Locate and identify every blood parasite.
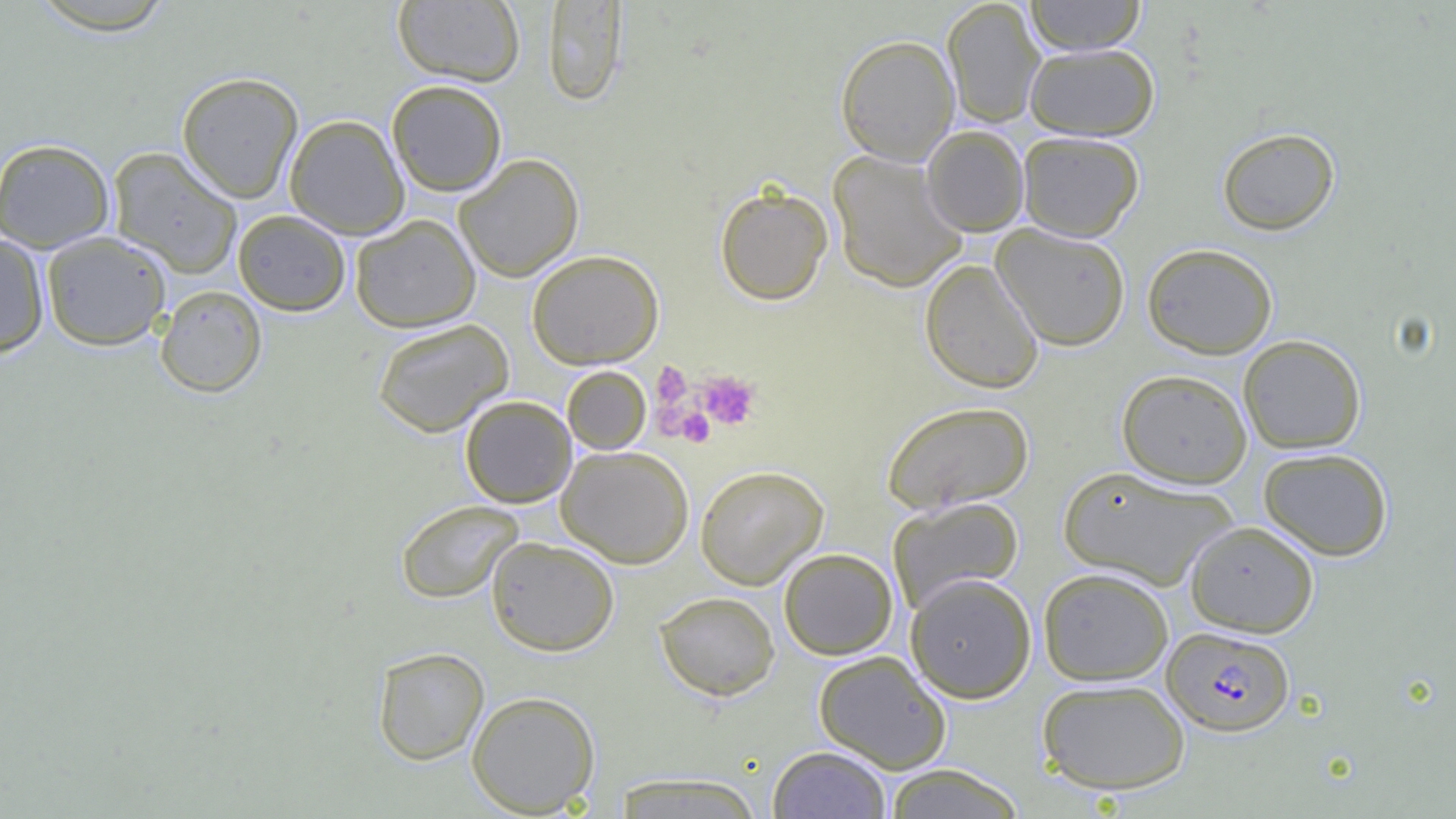

Approximate bounding boxes as [x1, y1, x2, y2] in pixels.
Plasmodium falciparum-infected red blood cells: [1163, 626, 1294, 736].
No Plasmodium ovale, Plasmodium malariae, Plasmodium vivax, Babesia divergens, or Trypanosoma brucei observed.

Uninfected red blood cell locations: [25, 0, 180, 36], [941, 0, 1045, 128], [1024, 0, 1147, 55], [392, 1, 525, 86], [542, 1, 628, 107], [835, 34, 960, 165], [1024, 43, 1159, 140], [176, 71, 304, 203], [386, 80, 507, 196], [285, 114, 409, 239], [922, 126, 1029, 236], [1216, 127, 1340, 236], [1017, 131, 1144, 242], [0, 138, 115, 252], [107, 146, 243, 279], [827, 150, 968, 292], [454, 153, 584, 282], [714, 184, 833, 305], [233, 209, 351, 315], [350, 214, 481, 333], [991, 223, 1131, 351], [40, 231, 172, 350], [0, 232, 50, 357], [1142, 242, 1278, 358], [526, 249, 664, 369], [920, 258, 1044, 394], [155, 285, 267, 398], [372, 319, 513, 437], [1238, 334, 1366, 453], [562, 366, 651, 455], [1117, 369, 1253, 488], [459, 395, 577, 508], [881, 400, 1035, 515], [556, 445, 694, 568], [1258, 447, 1393, 560], [695, 465, 829, 589], [1058, 465, 1237, 590], [886, 495, 1025, 614], [395, 499, 523, 604], [1185, 520, 1320, 637], [486, 536, 619, 656], [779, 548, 898, 660], [1038, 567, 1174, 685], [905, 573, 1037, 703], [654, 591, 780, 700], [372, 646, 490, 765], [813, 650, 951, 773], [1037, 679, 1190, 794], [466, 690, 601, 816], [767, 745, 891, 818], [882, 764, 1027, 818], [609, 771, 765, 818]. Platelet locations: [651, 362, 693, 410], [696, 370, 761, 430], [676, 408, 714, 448]. Slide-level diagnosis: Plasmodium falciparum. 1000x magnification. Image is 1456×819 pixels. Optical microscopy. One field of a larger specimen. Thin blood smear.